Locate every uninfected red blood cell.
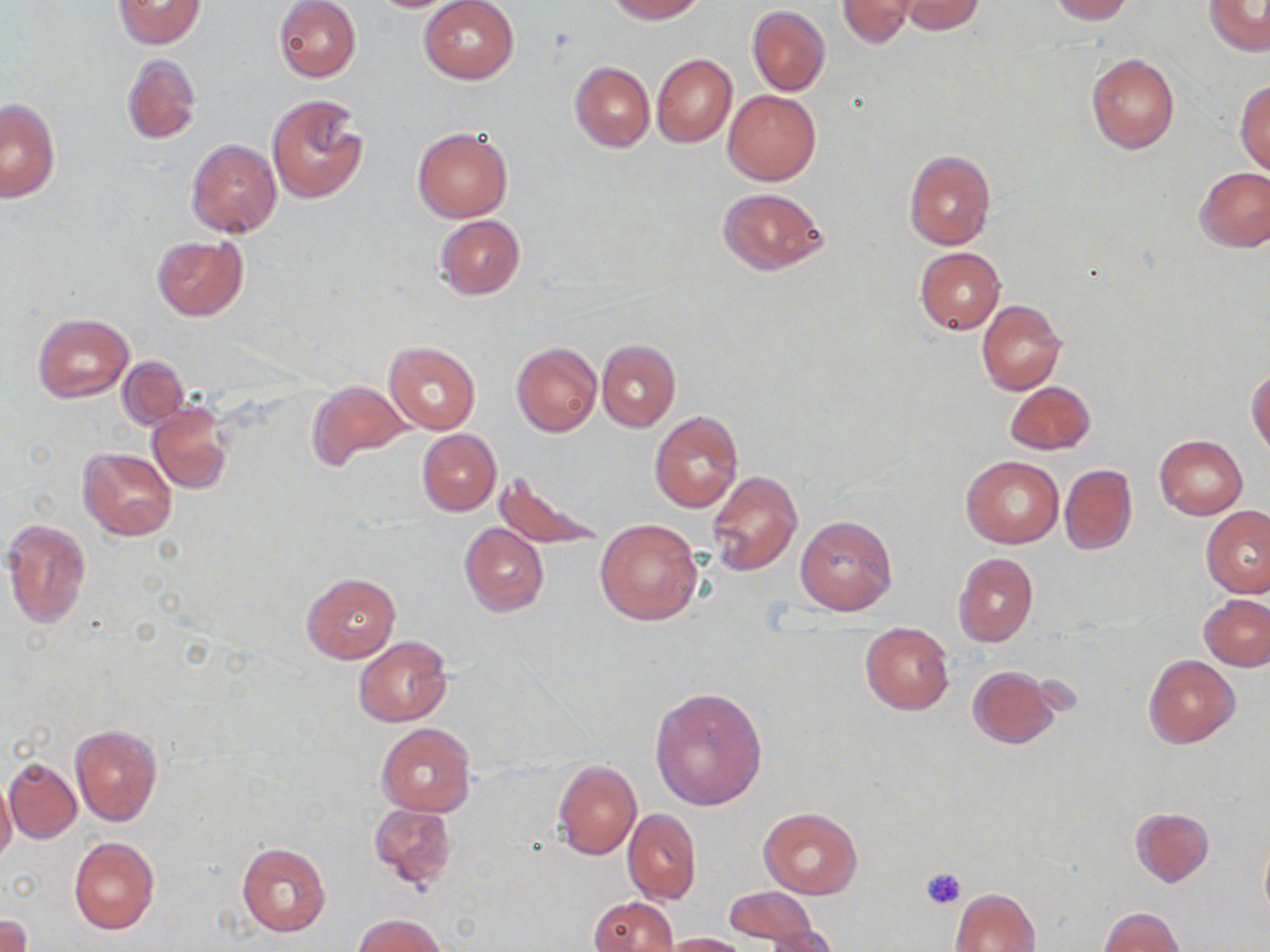

Approximate bounding boxes as [x1, y1, x2, y2] in pixels.
Uninfected red blood cells: [114, 0, 205, 49], [274, 0, 361, 82], [420, 0, 519, 84], [606, 0, 704, 22], [837, 0, 919, 47], [1046, 0, 1132, 23], [1205, 0, 1269, 55], [898, 1, 987, 35], [748, 6, 831, 97], [1086, 52, 1180, 154], [652, 53, 737, 147], [122, 54, 201, 145], [570, 61, 654, 152], [1236, 80, 1270, 175], [723, 89, 820, 185], [266, 92, 370, 203], [1, 98, 60, 201], [413, 127, 513, 222], [186, 139, 281, 237], [904, 149, 995, 250], [1195, 167, 1270, 252], [717, 187, 827, 276], [435, 215, 524, 300], [151, 235, 249, 321], [916, 247, 1005, 334], [977, 300, 1065, 395], [33, 313, 134, 404], [597, 339, 679, 432], [385, 341, 480, 434], [512, 343, 602, 438], [119, 357, 188, 429], [1247, 367, 1269, 455], [307, 381, 410, 469], [1005, 382, 1095, 455], [149, 403, 232, 494], [649, 411, 742, 512], [416, 430, 501, 515], [1154, 435, 1248, 520], [78, 448, 176, 540], [961, 456, 1063, 548], [1060, 464, 1137, 555], [493, 468, 606, 551], [706, 469, 802, 575], [1202, 505, 1270, 596], [795, 516, 896, 615], [3, 517, 91, 627], [595, 518, 703, 625], [459, 523, 549, 616], [953, 552, 1038, 646], [301, 572, 400, 662], [1200, 594, 1269, 670], [860, 623, 954, 715], [353, 637, 452, 727], [1143, 654, 1240, 749], [968, 666, 1058, 749], [650, 688, 767, 811], [376, 723, 476, 816], [70, 724, 162, 826], [3, 756, 81, 843], [553, 760, 641, 861], [0, 776, 17, 868], [370, 804, 456, 890], [759, 807, 863, 897], [1130, 807, 1214, 886], [624, 808, 701, 905], [1259, 834, 1270, 923], [69, 837, 160, 934], [236, 843, 331, 936], [724, 887, 821, 947], [952, 888, 1040, 952], [588, 896, 677, 952], [1099, 907, 1183, 952], [0, 914, 32, 952], [354, 914, 448, 951], [758, 925, 841, 952], [662, 933, 748, 952].

Summary:
  - Platelet locations: [920, 866, 967, 911]
  - Slide-level diagnosis: no evidence of blood parasites
  - Field of view: single
  - Preparation: thin blood film
  - Image size: 1270×952 pixels
  - Magnification: 1000x
  - Modality: optical microscopy
  - Stain: May-Grünwald-Giemsa